Classify this cell by malaria status.
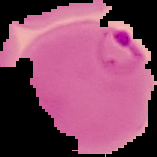
Parasitized.

{
  "image_type": "cell region segmented out of the field of view; surrounding area masked to black",
  "preparation": "thin blood film",
  "image_size": "157×157 pixels"
}